Identify the blood parasite species.
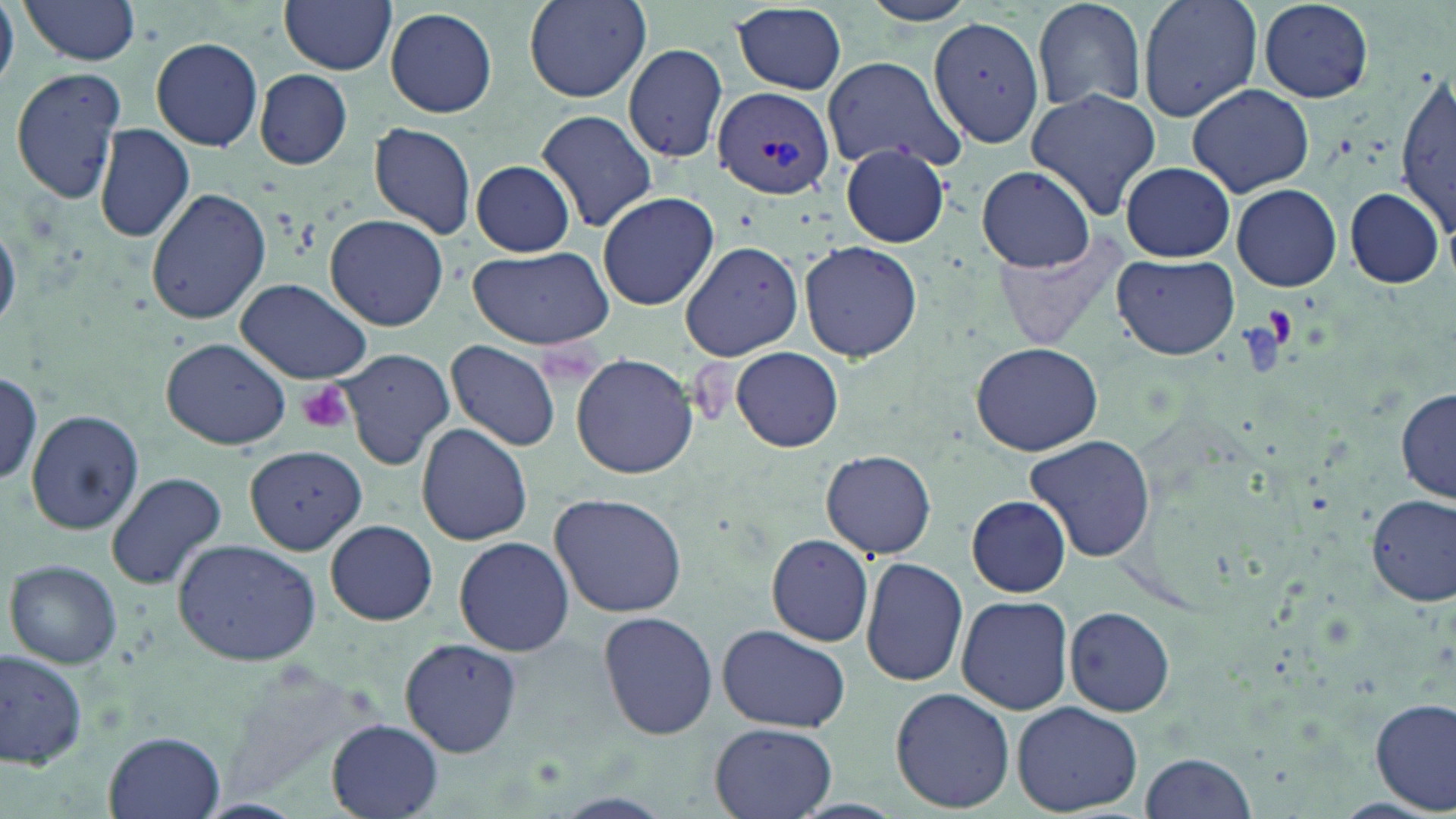

Plasmodium vivax.

Approximate bounding boxes as named x1/y1/x2/y2 corners in pixels. Plasmodium vivax-infected red blood cell locations: (x1=712, y1=85, x2=835, y2=201). Platelet locations: (x1=296, y1=382, x2=356, y2=435). Uninfected red blood cell locations: (x1=15, y1=0, x2=145, y2=65), (x1=279, y1=0, x2=398, y2=74), (x1=522, y1=0, x2=651, y2=104), (x1=862, y1=0, x2=980, y2=26), (x1=1031, y1=0, x2=1149, y2=114), (x1=1137, y1=0, x2=1263, y2=121), (x1=1257, y1=0, x2=1375, y2=102), (x1=0, y1=3, x2=18, y2=87), (x1=732, y1=4, x2=848, y2=94), (x1=384, y1=7, x2=498, y2=118), (x1=930, y1=16, x2=1047, y2=147), (x1=151, y1=36, x2=264, y2=151), (x1=623, y1=44, x2=729, y2=164), (x1=822, y1=57, x2=962, y2=171), (x1=10, y1=66, x2=127, y2=207), (x1=1397, y1=67, x2=1454, y2=243), (x1=255, y1=69, x2=353, y2=168), (x1=1186, y1=83, x2=1314, y2=196), (x1=1027, y1=89, x2=1163, y2=219), (x1=537, y1=109, x2=659, y2=233), (x1=369, y1=120, x2=478, y2=238), (x1=92, y1=124, x2=196, y2=243), (x1=842, y1=144, x2=950, y2=248), (x1=470, y1=161, x2=575, y2=256), (x1=1121, y1=162, x2=1235, y2=261), (x1=976, y1=165, x2=1098, y2=272), (x1=1231, y1=183, x2=1342, y2=291), (x1=1344, y1=187, x2=1447, y2=288), (x1=146, y1=188, x2=271, y2=325), (x1=597, y1=191, x2=719, y2=311), (x1=325, y1=213, x2=449, y2=331), (x1=0, y1=220, x2=20, y2=335), (x1=992, y1=231, x2=1133, y2=352), (x1=679, y1=239, x2=805, y2=362), (x1=801, y1=241, x2=922, y2=361), (x1=463, y1=246, x2=613, y2=349), (x1=1113, y1=252, x2=1240, y2=360), (x1=234, y1=277, x2=373, y2=384), (x1=162, y1=338, x2=293, y2=452), (x1=447, y1=340, x2=560, y2=454), (x1=971, y1=340, x2=1102, y2=457), (x1=730, y1=347, x2=844, y2=453), (x1=336, y1=349, x2=454, y2=469), (x1=570, y1=352, x2=698, y2=480), (x1=2, y1=371, x2=44, y2=487), (x1=1397, y1=388, x2=1455, y2=504), (x1=27, y1=409, x2=144, y2=534), (x1=416, y1=424, x2=533, y2=544), (x1=1025, y1=433, x2=1157, y2=563), (x1=244, y1=444, x2=364, y2=553), (x1=821, y1=449, x2=937, y2=560), (x1=105, y1=471, x2=229, y2=590), (x1=549, y1=491, x2=689, y2=618), (x1=1367, y1=493, x2=1455, y2=606), (x1=967, y1=494, x2=1069, y2=598), (x1=326, y1=519, x2=437, y2=625), (x1=766, y1=534, x2=873, y2=646), (x1=453, y1=535, x2=576, y2=657), (x1=172, y1=538, x2=321, y2=666), (x1=860, y1=557, x2=970, y2=687), (x1=5, y1=559, x2=123, y2=669), (x1=956, y1=594, x2=1073, y2=715), (x1=1063, y1=607, x2=1175, y2=716), (x1=597, y1=609, x2=719, y2=740), (x1=718, y1=623, x2=851, y2=733), (x1=400, y1=637, x2=522, y2=755), (x1=1, y1=648, x2=86, y2=771), (x1=214, y1=665, x2=380, y2=808), (x1=890, y1=687, x2=1015, y2=812), (x1=1371, y1=697, x2=1455, y2=815), (x1=1011, y1=700, x2=1144, y2=815), (x1=327, y1=720, x2=443, y2=817), (x1=708, y1=721, x2=839, y2=819), (x1=104, y1=731, x2=225, y2=818), (x1=1138, y1=751, x2=1259, y2=819). Light microscopy. Captured at 1000x magnification. Image is 1456×819 pixels. Thin blood smear. One field of a larger specimen. May-Grünwald-Giemsa-stained preparation.